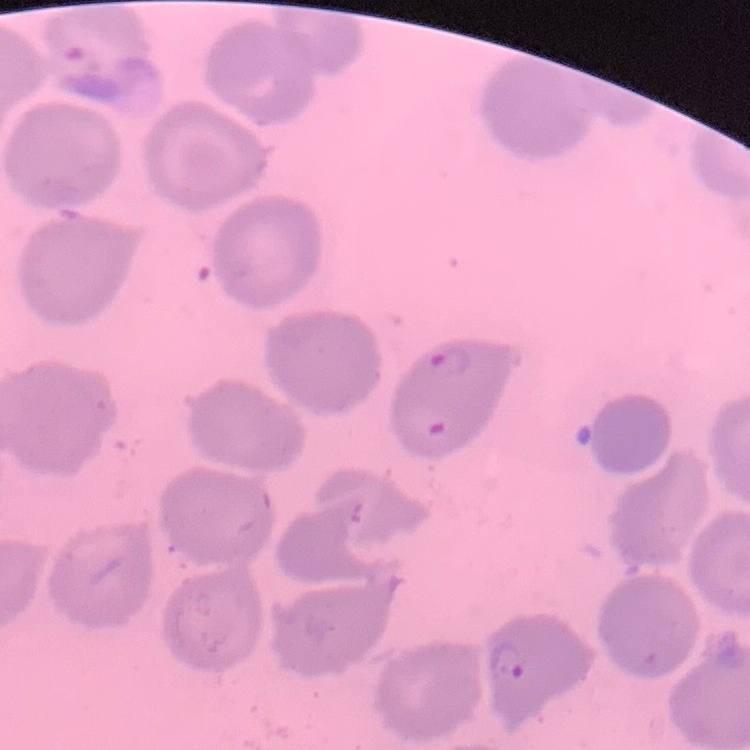
erythrocyte morphology = no rouleaux formation
image type = square crop of a larger photomicrograph
stain = Field's or Giemsa
preparation = thin peripheral smear